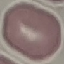
Malaria status: uninfected. Cell patch, automatically extracted from a larger field of view and resized to 64 × 64 pixels. Thin blood smear. Giemsa-stained preparation. Acquired by smartphone through the microscope eyepiece.